Identify the parasite.
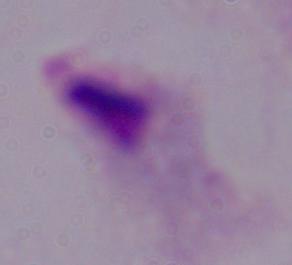

A trichomonad.

Captured at 1000x magnification. Micrograph.